Give the extent of all Plasmodium falciparum-infected red blood cells.
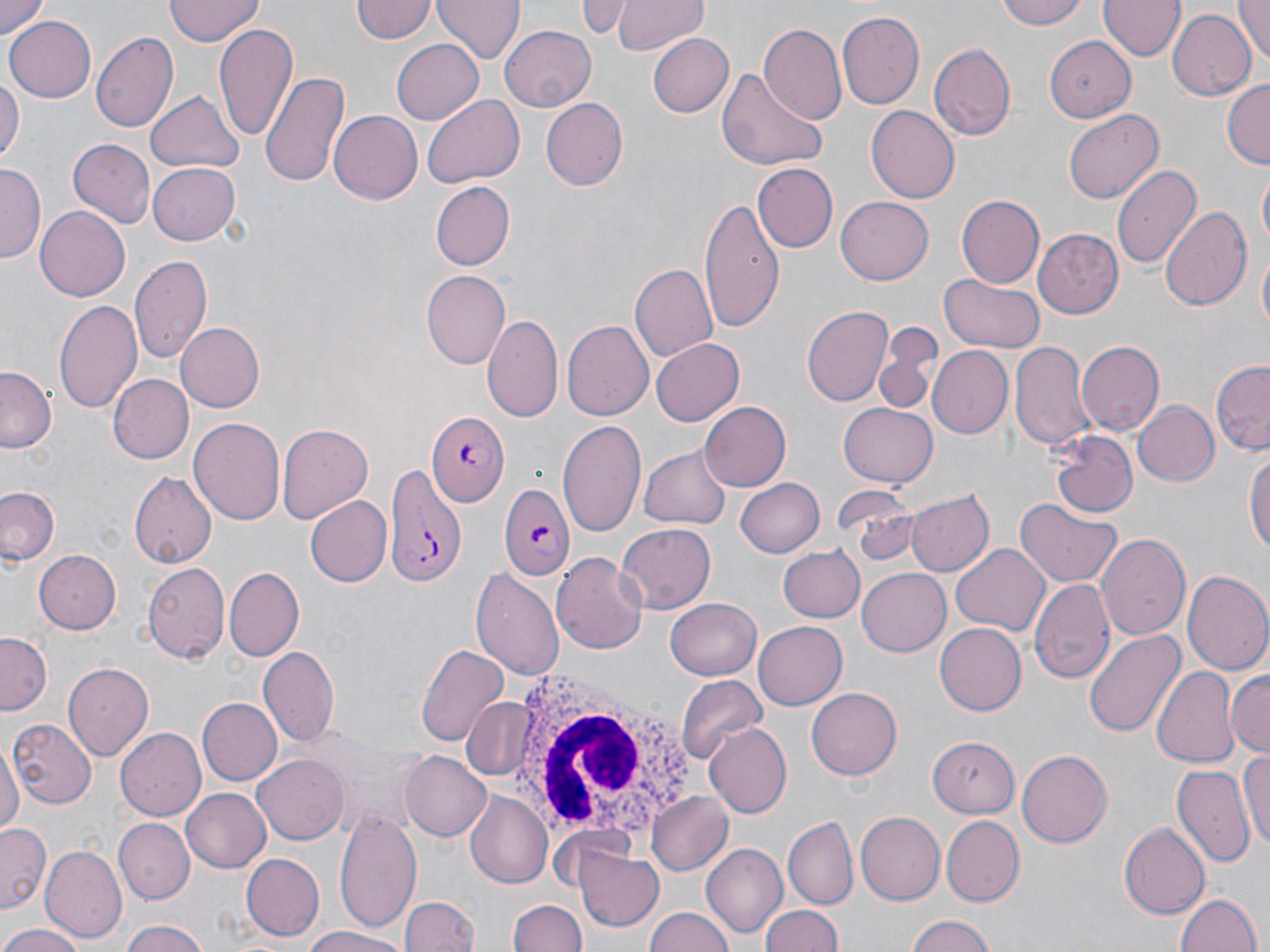

Approximate bounding boxes as (x1,y1)-(x2,y2) corner pairs in pixels.
Plasmodium falciparum-infected red blood cells: (426,412)-(510,504), (381,459)-(468,587), (499,484)-(574,580).

Summary:
  - White blood cell locations: (498,666)-(709,846)
  - Uninfected red blood cell locations: (1,0)-(51,39), (166,0)-(263,45), (434,0)-(526,66), (582,0)-(632,39), (613,0)-(707,55), (998,0)-(1089,29), (1230,0)-(1270,62), (1099,1)-(1183,62), (351,2)-(436,45), (837,10)-(925,111), (1167,10)-(1255,101), (4,15)-(94,103), (757,21)-(847,127), (215,23)-(296,139), (501,25)-(596,110), (90,31)-(178,133), (646,32)-(734,118), (391,36)-(484,123), (1041,36)-(1139,121), (929,42)-(1016,141), (717,66)-(827,174), (262,70)-(348,186), (0,75)-(22,171), (1222,79)-(1269,170), (147,92)-(245,175), (422,95)-(523,188), (539,98)-(625,190), (866,106)-(958,204), (328,109)-(421,201), (1063,109)-(1163,205), (69,138)-(155,228), (147,162)-(241,245), (1112,163)-(1201,269), (754,164)-(837,253), (0,166)-(42,262), (1257,168)-(1270,252), (431,182)-(515,270), (956,194)-(1045,288), (700,195)-(786,336), (836,197)-(933,285), (35,206)-(131,300), (1161,206)-(1255,310), (1034,229)-(1123,320), (1255,250)-(1269,342), (129,255)-(211,366), (630,264)-(718,364), (420,271)-(511,370), (939,274)-(1042,352), (53,298)-(142,413), (803,304)-(894,405), (482,313)-(562,421), (562,319)-(652,420), (875,322)-(945,412), (177,323)-(264,410), (648,338)-(743,426), (1011,340)-(1092,452), (1076,340)-(1163,434), (930,346)-(1014,437), (1212,359)-(1270,454), (0,368)-(55,455), (107,374)-(194,465), (1133,399)-(1219,487), (838,400)-(936,487), (699,403)-(790,490), (190,417)-(286,525), (556,417)-(649,537), (276,424)-(372,523), (1049,432)-(1137,516), (1245,445)-(1270,565), (640,447)-(731,529), (130,473)-(215,569), (736,477)-(826,558), (0,486)-(61,566), (832,487)-(921,566), (905,489)-(993,577), (305,496)-(392,586), (1017,499)-(1121,588), (615,523)-(716,615), (1097,533)-(1191,640), (953,544)-(1049,635), (776,545)-(865,624), (31,548)-(120,636), (552,552)-(645,653), (144,565)-(231,663), (469,565)-(564,681), (1181,567)-(1270,677), (224,568)-(303,661), (857,568)-(954,656), (1028,579)-(1115,687), (666,596)-(764,681), (753,620)-(846,710), (933,623)-(1026,715), (1082,629)-(1184,739), (0,632)-(50,713), (417,640)-(509,745), (258,648)-(337,745), (63,663)-(152,760), (1150,664)-(1238,767), (1227,669)-(1270,757), (676,674)-(767,766), (807,688)-(902,780), (458,697)-(540,782), (198,698)-(282,785), (9,719)-(96,807), (706,721)-(793,817), (117,727)-(204,819), (925,734)-(1020,818), (1,741)-(20,842), (1018,750)-(1113,847), (1239,751)-(1270,850), (401,752)-(493,841), (254,753)-(351,845), (1172,763)-(1255,870), (182,788)-(270,872), (646,790)-(733,877), (465,793)-(553,886), (335,807)-(421,932), (853,812)-(942,904), (941,816)-(1026,907), (783,817)-(858,907), (114,820)-(193,902), (1119,822)-(1210,919), (1,824)-(50,913), (700,843)-(787,938), (42,845)-(127,942), (575,848)-(665,931), (239,853)-(324,941), (1174,890)-(1264,952), (402,894)-(476,952), (511,898)-(588,952), (759,905)-(847,952), (645,908)-(732,952), (904,913)-(999,952), (120,920)-(214,952), (0,925)-(90,952), (302,927)-(414,951)
  - Slide-level diagnosis: Plasmodium falciparum
  - Preparation: thin blood smear
  - Magnification: 1000x
  - Field of view: one of a larger specimen
  - Modality: light microscopy
  - Stain: May-Grünwald-Giemsa
  - Image size: 1270×952 pixels